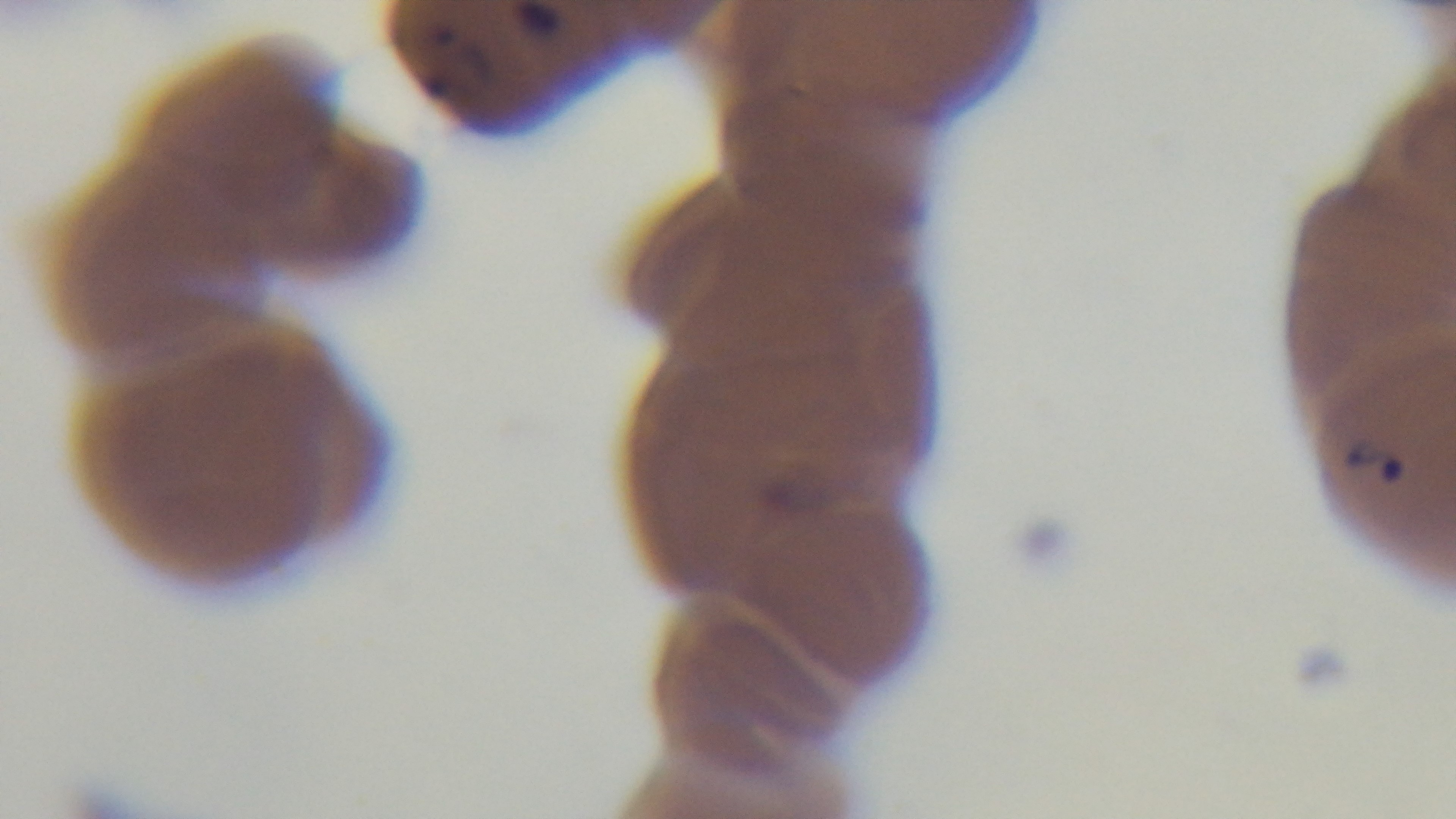
stain: Giemsa
preparation: thin smear
modality: light microscopy
malaria_status: positive
objective: 100x oil immersion
field_of_view: single
capture: mounted 4K digital camera